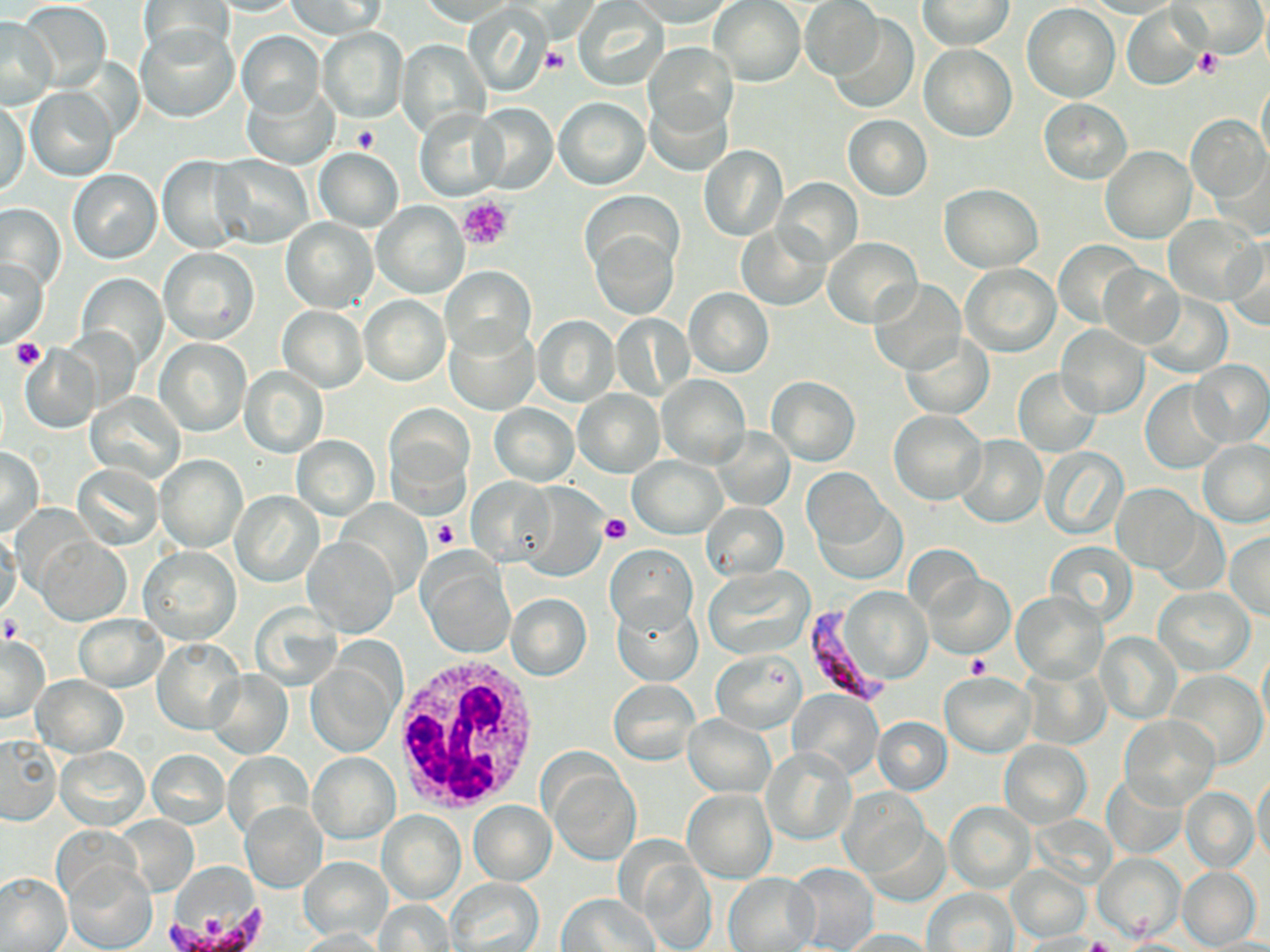
slide-level diagnosis = Plasmodium falciparum
stain = May-Grünwald-Giemsa
magnification = 1000x
white blood cell locations = approximate bounding boxes as (x1,y1)-(x2,y2) corner pairs in pixels: (389,651)-(541,817)
modality = light microscopy
image size = 1270×952 pixels
platelet locations = approximate bounding boxes as (x1,y1)-(x2,y2) corner pairs in pixels: (539,46)-(568,74), (1195,47)-(1223,77), (352,124)-(378,154), (458,195)-(513,252), (10,339)-(46,369), (597,513)-(631,543), (430,519)-(461,551), (1,617)-(23,646), (967,654)-(993,679), (1087,935)-(1115,952)
preparation = thin blood film
Plasmodium falciparum-infected red blood cell locations = approximate bounding boxes as (x1,y1)-(x2,y2) corner pairs in pixels: (807,604)-(889,703), (166,905)-(272,950)
uninfected red blood cell locations = approximate bounding boxes as (x1,y1)-(x2,y2) corner pairs in pixels: (200,0)-(301,16), (287,0)-(386,38), (919,0)-(1014,50), (1174,0)-(1265,58), (137,1)-(234,62), (415,1)-(521,26), (630,1)-(740,27), (710,1)-(805,87), (801,1)-(885,81), (1085,1)-(1181,18), (18,2)-(112,91), (574,2)-(668,90), (465,3)-(554,97), (1023,4)-(1121,102), (1121,4)-(1207,90), (829,15)-(918,114), (0,17)-(56,109), (135,25)-(239,122), (317,27)-(408,124), (236,30)-(326,119), (395,39)-(491,141), (643,42)-(738,142), (919,45)-(1016,142), (1257,75)-(1270,169), (241,81)-(339,170), (643,84)-(735,174), (26,87)-(118,182), (555,97)-(649,189), (1,99)-(30,199), (1038,99)-(1132,184), (473,103)-(557,194), (416,106)-(507,202), (842,114)-(932,200), (1185,115)-(1268,205), (699,145)-(787,241), (1101,146)-(1196,243), (313,148)-(404,231), (158,154)-(249,253), (210,154)-(315,247), (69,169)-(162,264), (775,180)-(860,265), (940,183)-(1044,272), (373,201)-(467,297), (0,205)-(64,294), (1164,215)-(1261,303), (280,217)-(377,312), (737,223)-(828,311), (587,224)-(680,319), (1222,235)-(1270,328), (822,237)-(922,327), (1053,242)-(1142,327), (159,247)-(258,344), (2,259)-(48,347), (962,263)-(1059,356), (1097,263)-(1184,349), (441,266)-(534,359), (78,275)-(167,365), (867,279)-(966,376), (685,288)-(774,377), (1141,292)-(1231,378), (360,295)-(449,385), (277,306)-(368,391), (610,313)-(694,400), (532,315)-(619,406), (446,323)-(539,414), (1057,325)-(1150,418), (63,326)-(140,411), (900,334)-(993,420), (155,337)-(251,437), (20,344)-(101,434), (1188,361)-(1269,448), (242,367)-(327,457), (1012,368)-(1102,458), (657,374)-(749,468), (768,376)-(860,466), (1139,380)-(1229,473), (574,389)-(665,476), (86,391)-(184,482), (488,403)-(579,484), (385,407)-(473,510), (889,410)-(986,505), (713,427)-(795,509), (955,435)-(1046,527), (292,436)-(378,518), (1199,439)-(1270,527), (0,447)-(43,534), (1039,447)-(1129,540), (156,455)-(245,551), (630,455)-(725,537), (73,465)-(162,549), (803,471)-(897,570), (468,478)-(557,566), (512,483)-(609,579), (1113,484)-(1202,573), (231,491)-(325,587), (702,502)-(788,579), (0,532)-(22,621), (1225,532)-(1270,619), (38,537)-(129,626), (303,537)-(399,636), (1045,542)-(1137,628), (606,545)-(696,633), (139,546)-(241,644), (417,550)-(514,659), (704,565)-(814,658), (924,573)-(1013,658), (1152,586)-(1255,675), (832,589)-(935,690), (1011,591)-(1106,683), (505,594)-(591,680), (612,598)-(701,686), (74,614)-(167,692), (1095,631)-(1181,724), (0,634)-(49,722), (152,639)-(243,734), (1258,643)-(1270,740), (307,652)-(402,756), (711,652)-(804,733), (1021,662)-(1111,751), (1166,669)-(1267,767), (940,671)-(1036,757), (205,672)-(292,758), (33,675)-(127,756), (610,678)-(701,766), (790,690)-(882,780), (683,713)-(776,797), (1120,715)-(1220,810), (873,716)-(952,795), (0,735)-(61,825), (999,739)-(1091,829), (56,746)-(148,829), (762,748)-(855,845), (147,750)-(230,829), (227,751)-(313,843), (308,751)-(399,843), (545,765)-(640,864), (1252,771)-(1270,866), (1102,772)-(1188,858), (1182,786)-(1257,872), (683,788)-(775,883), (838,788)-(929,876), (241,800)-(328,892), (469,800)-(556,886), (944,801)-(1035,891), (376,811)-(466,905), (113,813)-(198,897), (864,822)-(949,906), (1093,852)-(1185,943), (637,855)-(718,952), (299,857)-(392,943), (63,859)-(157,952), (785,864)-(879,952), (1007,866)-(1090,942), (1177,866)-(1262,949), (0,874)-(71,952), (724,874)-(817,951), (447,878)-(544,952), (925,888)-(1018,951), (557,894)-(659,951), (374,899)-(455,950), (296,928)-(387,952), (841,929)-(938,951), (1020,934)-(1109,952), (1194,937)-(1270,952)
field of view = single